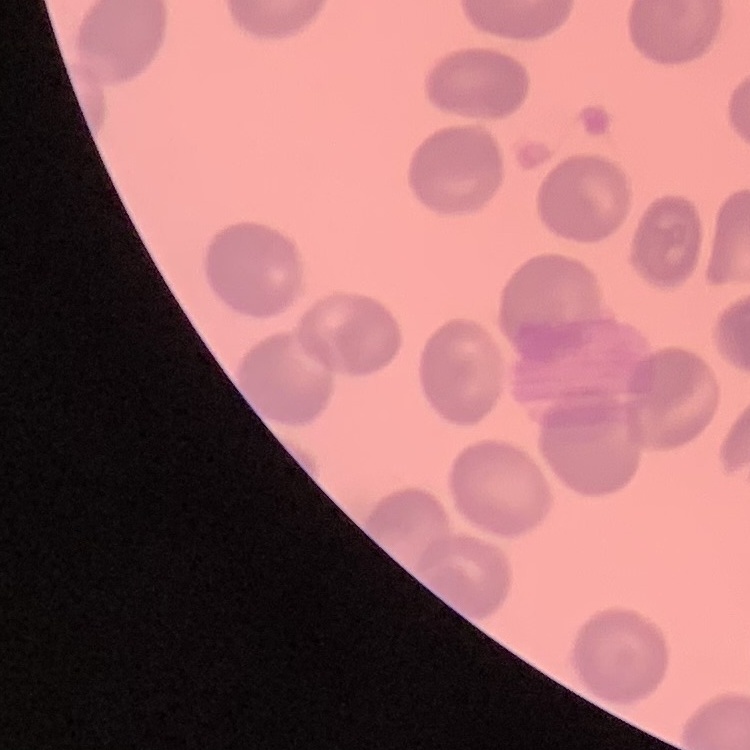
The red blood cells exhibit no rouleaux formation. Field's or Giemsa stain. Square crop of a larger photomicrograph. Thin blood smear.